Describe the morphology of the erythrocytes.
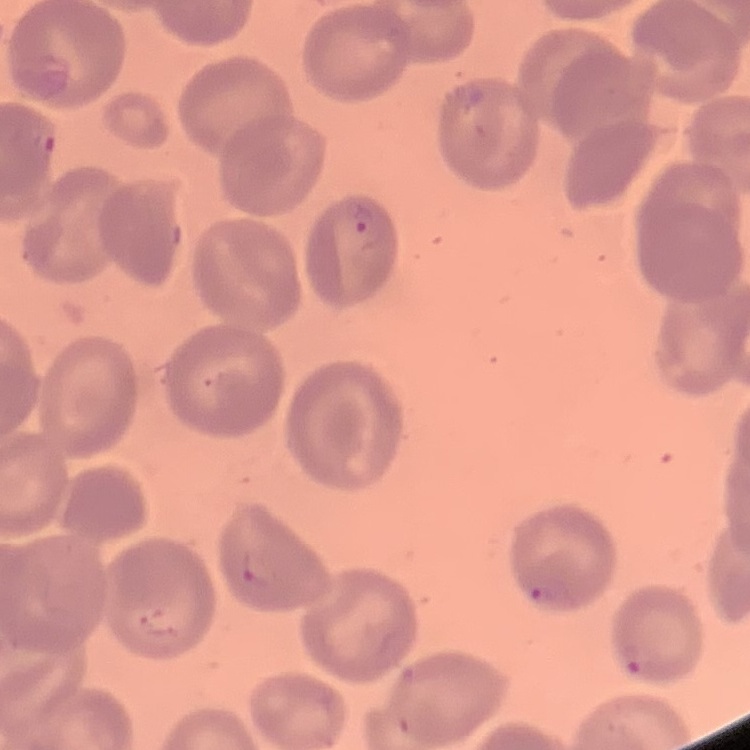

They show no rouleaux formation.

preparation: thin blood smear
stain: Field's or Giemsa
image_type: one tile cut from a larger photomicrograph